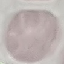

Result: no malaria parasites seen. Acquired by smartphone through the microscope eyepiece. Thin blood smear. Cell patch, automatically extracted from a larger field of view and resized to 64 × 64 pixels. Giemsa stain.